Assess the morphology of the red blood cells.
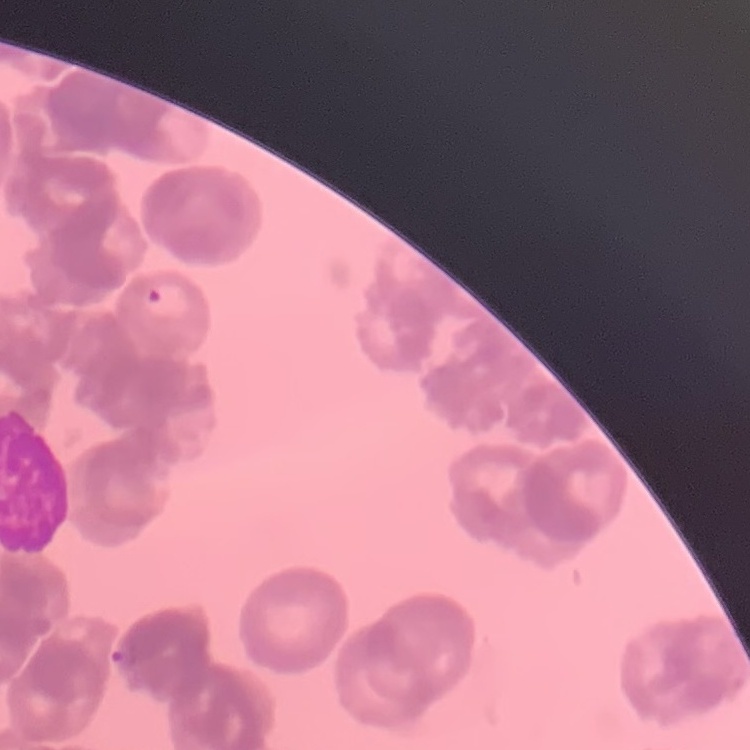
They show rouleaux formation.

image_type: square crop of a larger photomicrograph
preparation: thin blood smear
stain: Field's or Giemsa